Identify the preparation type.
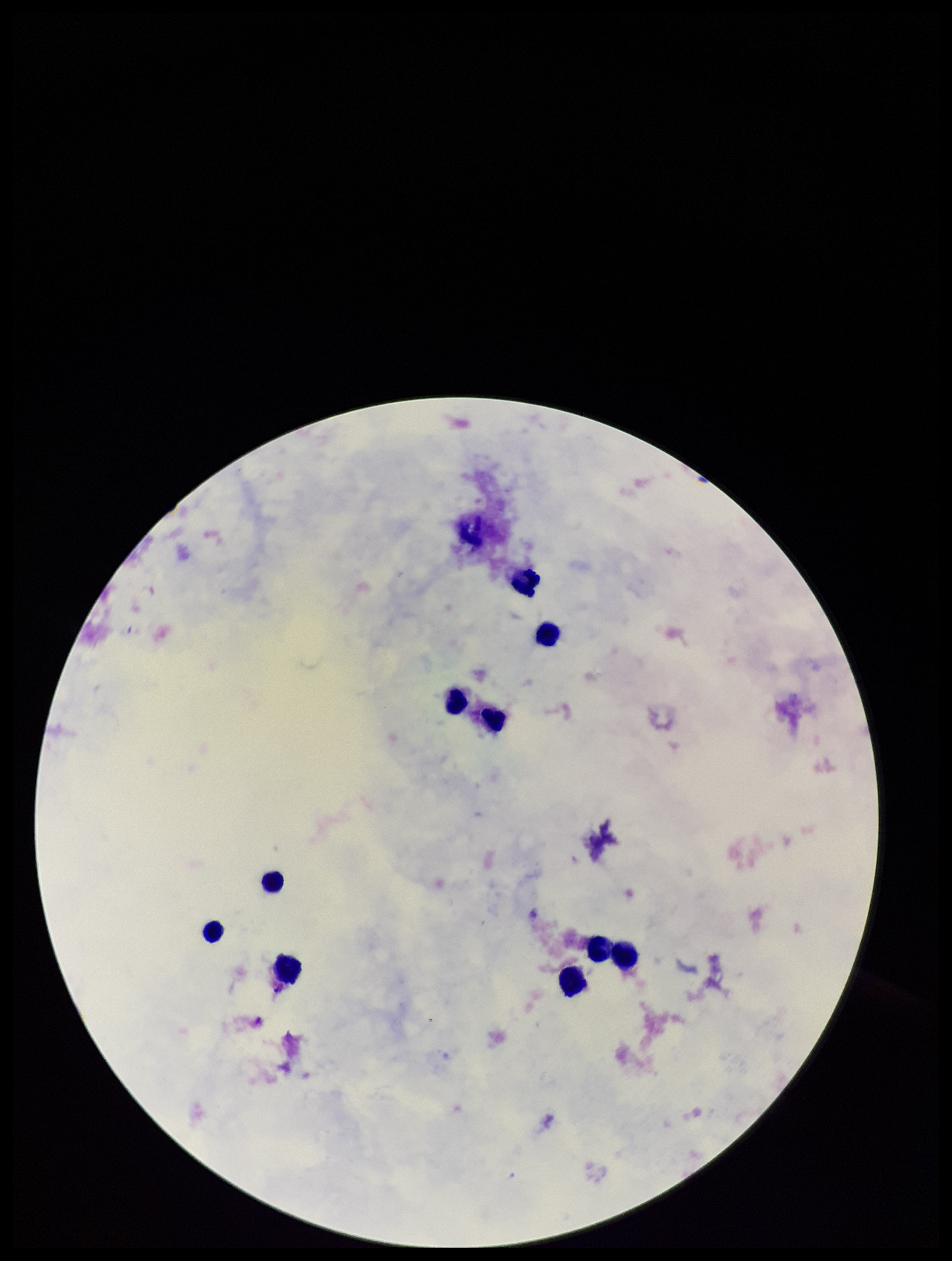

Thick.

parasite count = 0
image size = 952×1261 pixels
patient malaria status = negative
capture = smartphone photograph through the microscope eyepiece
leukocyte count = 10
field of view = single
Plasmodium parasites = none identified
stain = Giemsa